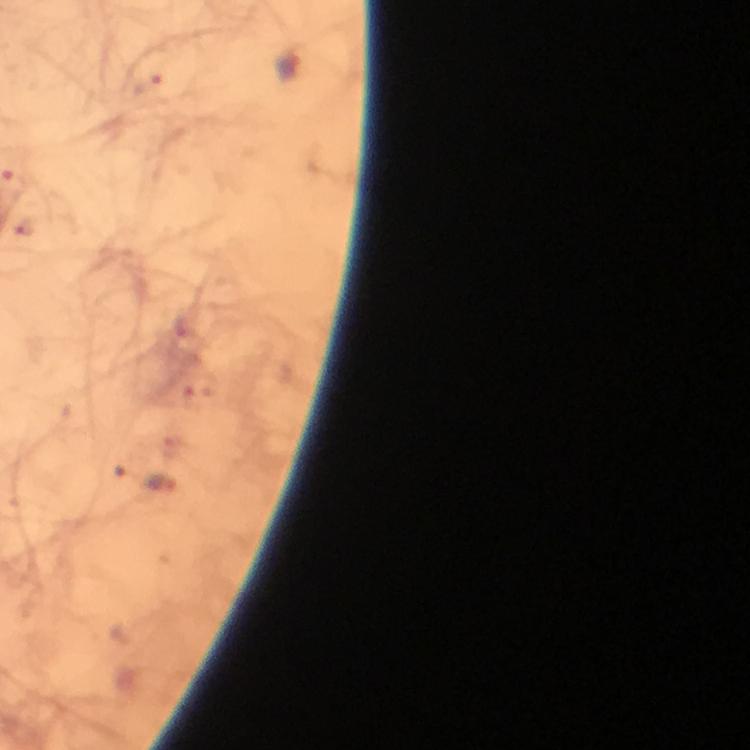 Approximate centers as (x, y) in pixels. Plasmodium parasite locations: (290, 69), (161, 487). Cropped region of a single field of view. Image is 750×750 pixels. Immersion oil applied. From a malaria diagnostic workup. At 100x magnification. Smartphone photograph taken through a microscope. Giemsa-stained preparation. Thick smear.